Locate Plasmodium parasites and leukocytes.
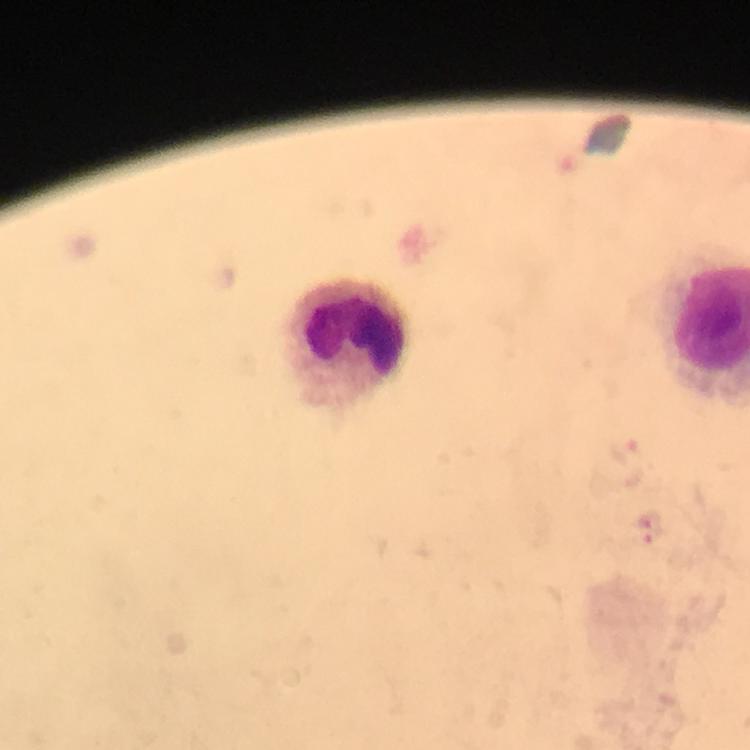

Approximate centers as {x, y} in pixels.
Plasmodium parasites: {647, 527}.
Leukocytes: {347, 347}.

Image is 750×750 pixels. A crop from one field of view. Thick smear. Giemsa-stained preparation. 100x magnification. From a malaria diagnostic workup. Photographed with a smartphone mounted on the microscope. Immersion oil was used.